Comment on the morphology of the erythrocytes.
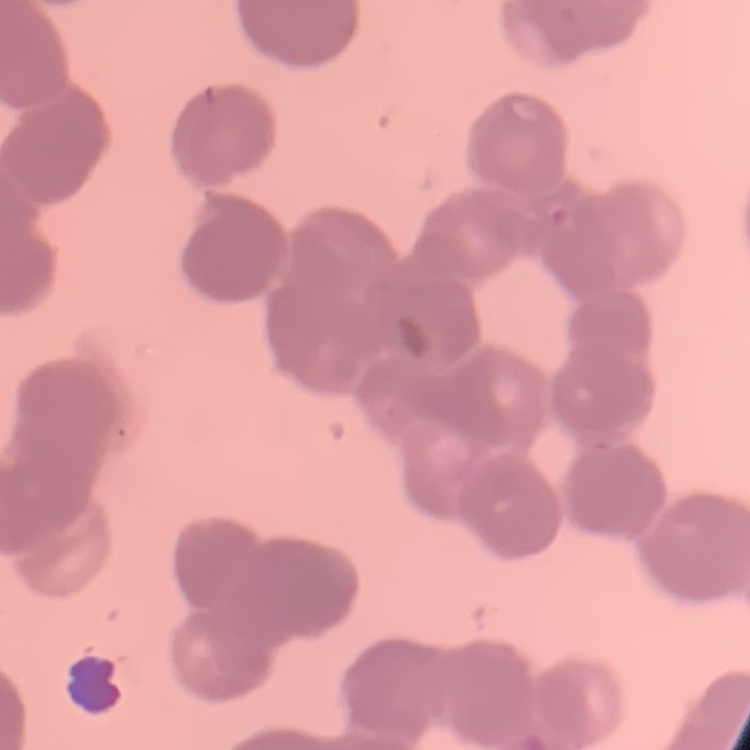

They show rouleaux formation.

One tile cut from a larger photomicrograph. Field's or Giemsa stain. Thin blood film.